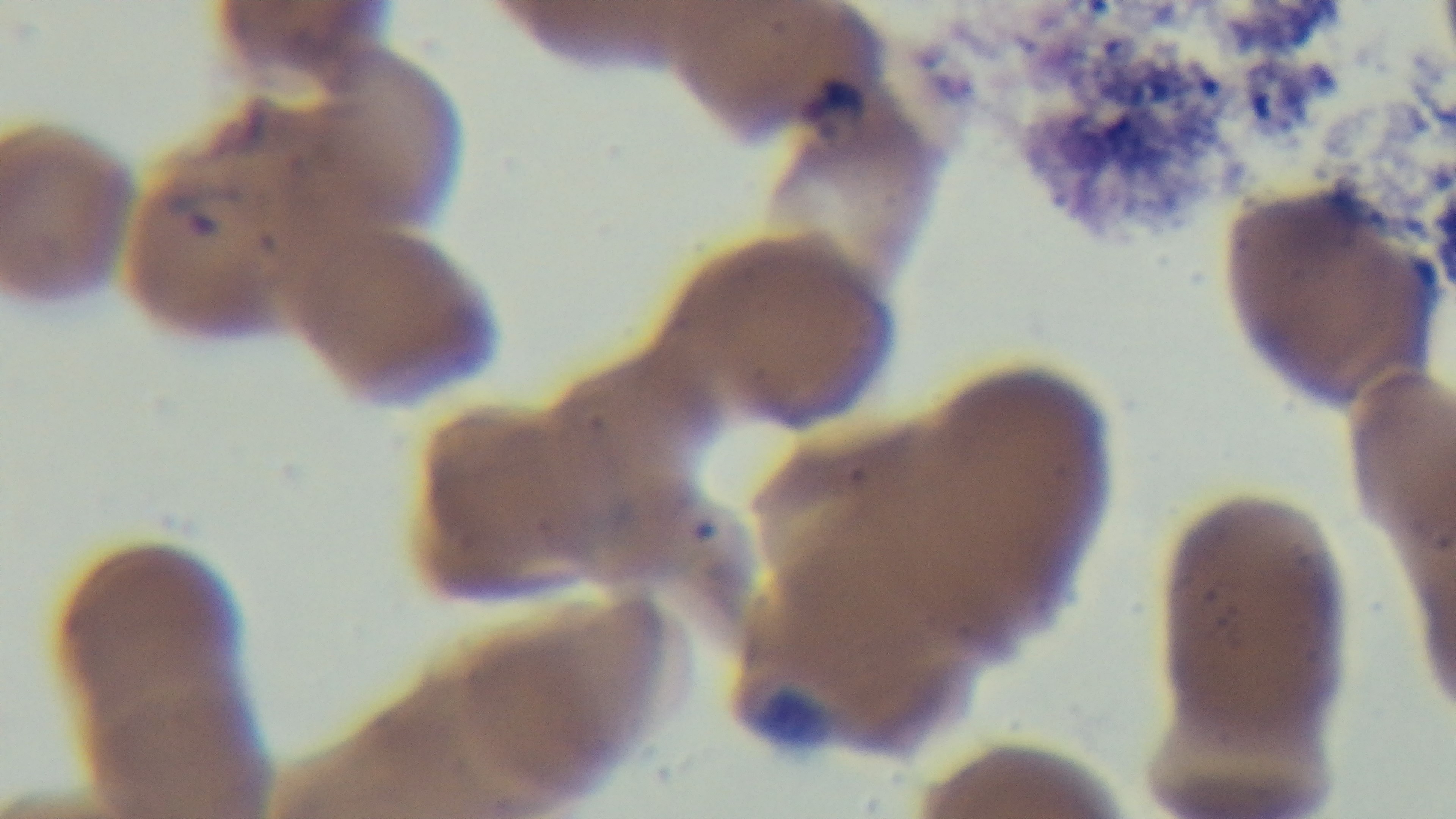 Captured with a mounted 4K digital camera. Oil-immersion objective, 100x. Single field of view. Preparation: thin blood film. Light microscopy. Malaria status: infected. Giemsa stain.